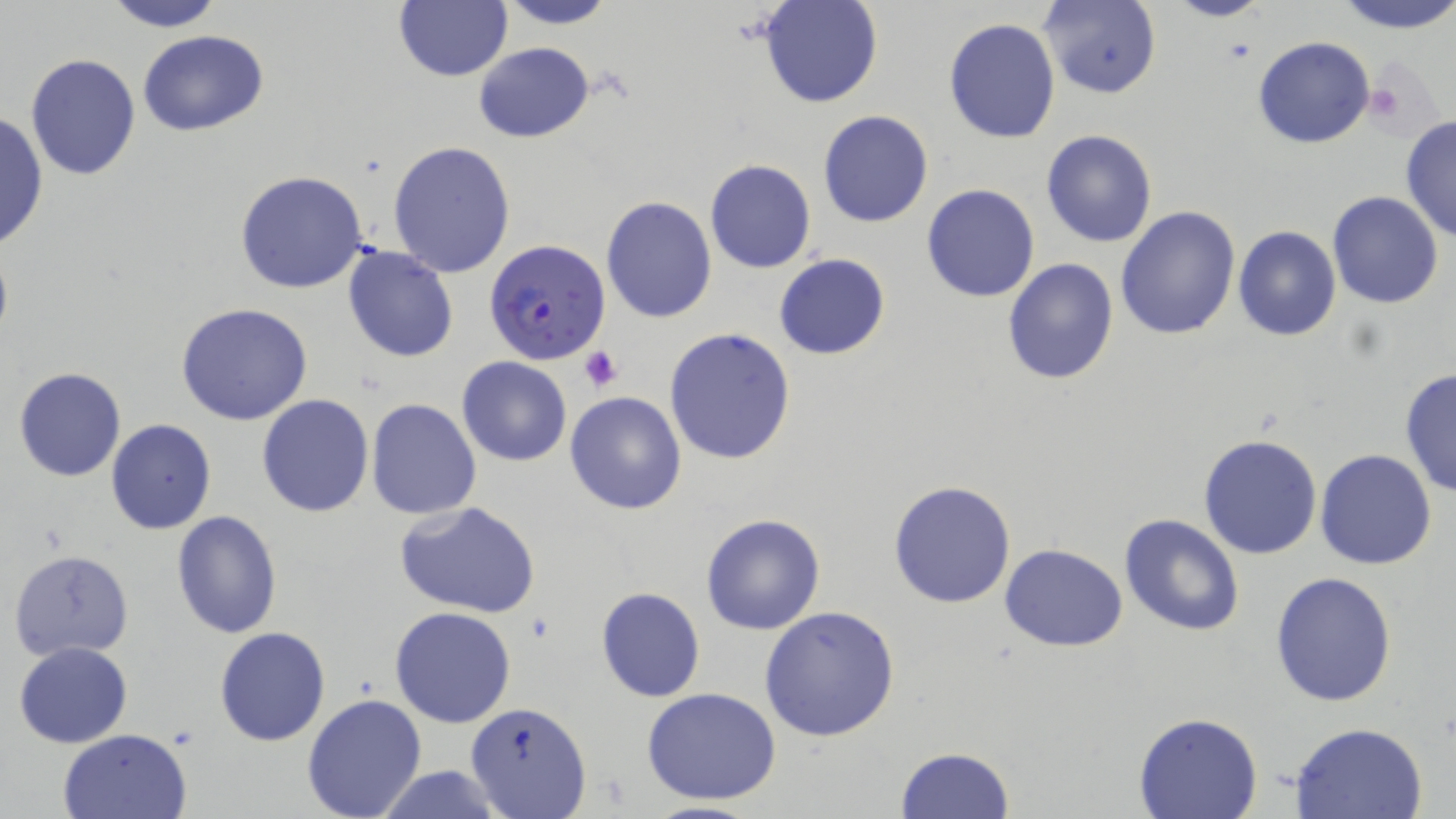

Approximate bounding boxes as named x1/y1/x2/y2 corners in pixels. Uninfected red blood cell locations: (x1=100, y1=0, x2=225, y2=31), (x1=493, y1=0, x2=619, y2=30), (x1=759, y1=0, x2=884, y2=108), (x1=1161, y1=0, x2=1270, y2=24), (x1=1330, y1=0, x2=1456, y2=34), (x1=393, y1=2, x2=513, y2=82), (x1=1039, y1=2, x2=1162, y2=98), (x1=943, y1=18, x2=1061, y2=143), (x1=137, y1=29, x2=268, y2=136), (x1=1252, y1=36, x2=1376, y2=149), (x1=473, y1=41, x2=595, y2=142), (x1=25, y1=53, x2=141, y2=180), (x1=818, y1=109, x2=933, y2=228), (x1=1, y1=111, x2=48, y2=253), (x1=1399, y1=117, x2=1456, y2=244), (x1=1042, y1=130, x2=1157, y2=247), (x1=388, y1=141, x2=516, y2=278), (x1=705, y1=160, x2=815, y2=273), (x1=234, y1=171, x2=369, y2=294), (x1=920, y1=183, x2=1040, y2=303), (x1=1329, y1=191, x2=1443, y2=309), (x1=600, y1=195, x2=717, y2=323), (x1=1115, y1=204, x2=1240, y2=340), (x1=1233, y1=227, x2=1341, y2=341), (x1=342, y1=245, x2=459, y2=363), (x1=773, y1=253, x2=890, y2=359), (x1=1003, y1=259, x2=1118, y2=386), (x1=175, y1=304, x2=315, y2=426), (x1=664, y1=328, x2=797, y2=466), (x1=458, y1=357, x2=571, y2=467), (x1=14, y1=367, x2=126, y2=481), (x1=1398, y1=367, x2=1456, y2=498), (x1=565, y1=391, x2=688, y2=515), (x1=256, y1=394, x2=375, y2=517), (x1=366, y1=399, x2=482, y2=519), (x1=105, y1=420, x2=216, y2=534), (x1=1198, y1=433, x2=1322, y2=559), (x1=1315, y1=449, x2=1436, y2=570), (x1=887, y1=480, x2=1017, y2=609), (x1=392, y1=500, x2=543, y2=620), (x1=171, y1=510, x2=282, y2=641), (x1=1119, y1=513, x2=1245, y2=637), (x1=698, y1=514, x2=826, y2=636), (x1=999, y1=543, x2=1128, y2=651), (x1=9, y1=548, x2=133, y2=660), (x1=1270, y1=571, x2=1398, y2=707), (x1=596, y1=587, x2=705, y2=703), (x1=757, y1=604, x2=901, y2=742), (x1=390, y1=606, x2=516, y2=728), (x1=214, y1=628, x2=331, y2=746), (x1=13, y1=642, x2=132, y2=748), (x1=642, y1=688, x2=783, y2=805), (x1=302, y1=694, x2=426, y2=819), (x1=465, y1=703, x2=591, y2=818), (x1=1132, y1=713, x2=1262, y2=819), (x1=1289, y1=721, x2=1430, y2=818), (x1=58, y1=728, x2=191, y2=818), (x1=895, y1=746, x2=1016, y2=818), (x1=374, y1=765, x2=505, y2=819), (x1=636, y1=801, x2=772, y2=819). Platelet locations: (x1=1364, y1=75, x2=1415, y2=127), (x1=580, y1=346, x2=623, y2=392), (x1=526, y1=612, x2=557, y2=644). Plasmodium falciparum-infected red blood cell locations: (x1=486, y1=238, x2=610, y2=365). Slide-level diagnosis: Plasmodium falciparum. Single field of view. Captured at 1000x magnification. Image is 1456×819 pixels. May-Grünwald-Giemsa-stained preparation. Optical microscopy. Thin blood smear.